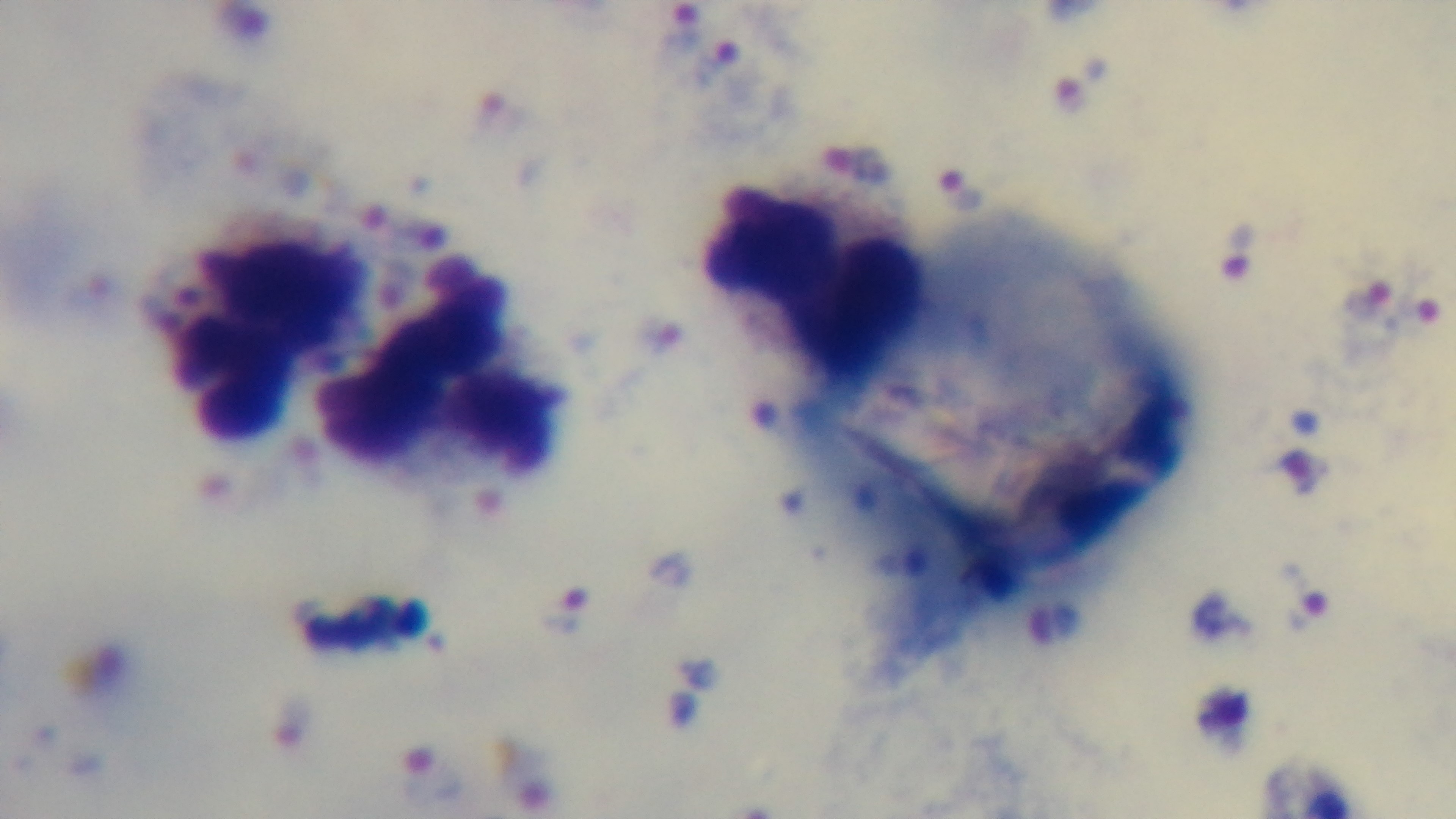
modality: light microscopy
objective: 100x oil immersion
capture: mounted 4K digital camera
field_of_view: one from the slide
stain: Giemsa
malaria_status: positive
preparation: thick